Give the extent of all Plasmodium falciparum-infected red blood cells.
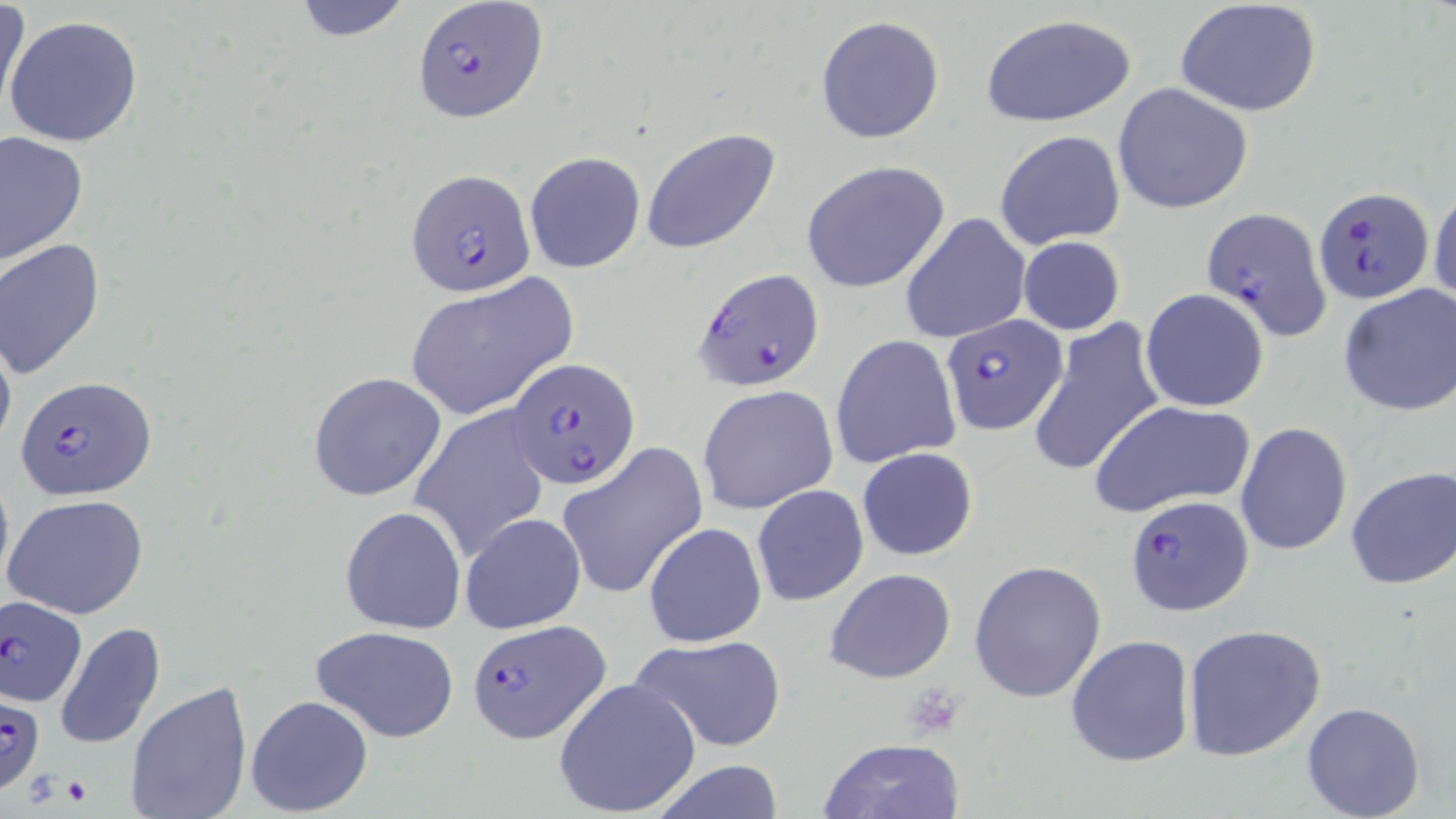
Approximate bounding boxes as (x1,y1)-(x2,y2) corner pairs in pixels.
Plasmodium falciparum-infected red blood cells: (411,0)-(549,124), (406,169)-(537,297), (1315,187)-(1432,304), (1201,206)-(1330,341), (693,266)-(825,393), (940,312)-(1068,436), (507,356)-(641,491), (14,376)-(157,502), (1125,495)-(1256,616), (0,594)-(88,707), (466,618)-(609,743), (0,698)-(47,794).

Uninfected red blood cell locations: (0,0)-(28,125), (288,0)-(415,42), (1174,0)-(1323,118), (979,13)-(1137,126), (4,15)-(144,147), (814,15)-(945,144), (1112,82)-(1255,215), (642,127)-(781,255), (1,130)-(90,266), (994,130)-(1126,248), (525,151)-(646,273), (801,161)-(949,291), (1429,186)-(1456,311), (901,213)-(1030,344), (1017,235)-(1126,336), (1,239)-(110,381), (405,277)-(575,420), (1338,283)-(1455,417), (1140,289)-(1269,413), (1026,317)-(1166,479), (0,323)-(17,460), (831,334)-(963,469), (307,371)-(447,503), (697,384)-(839,516), (1087,397)-(1257,518), (409,406)-(551,559), (1235,421)-(1354,556), (556,442)-(708,601), (856,446)-(979,562), (0,461)-(14,603), (1344,466)-(1456,591), (751,483)-(869,606), (4,493)-(151,620), (340,506)-(467,634), (460,512)-(586,635), (643,522)-(765,649), (969,560)-(1106,703), (824,568)-(957,684), (54,622)-(166,750), (1184,623)-(1327,762), (311,625)-(460,743), (631,634)-(787,753), (1064,634)-(1195,768), (553,678)-(702,818), (124,681)-(254,819), (246,694)-(374,817), (1302,702)-(1427,819), (818,735)-(964,819), (645,761)-(789,817). Platelet locations: (906,689)-(963,733), (61,775)-(92,806). Slide-level diagnosis: Plasmodium falciparum. Light microscopy. Captured at 1000x magnification. Thin blood smear. Single field of view. Image is 1456×819 pixels. May-Grünwald-Giemsa stain.